Identify the parasite.
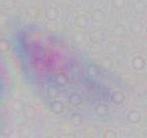
Toxoplasma gondii.

magnification = 1000x
modality = micrograph